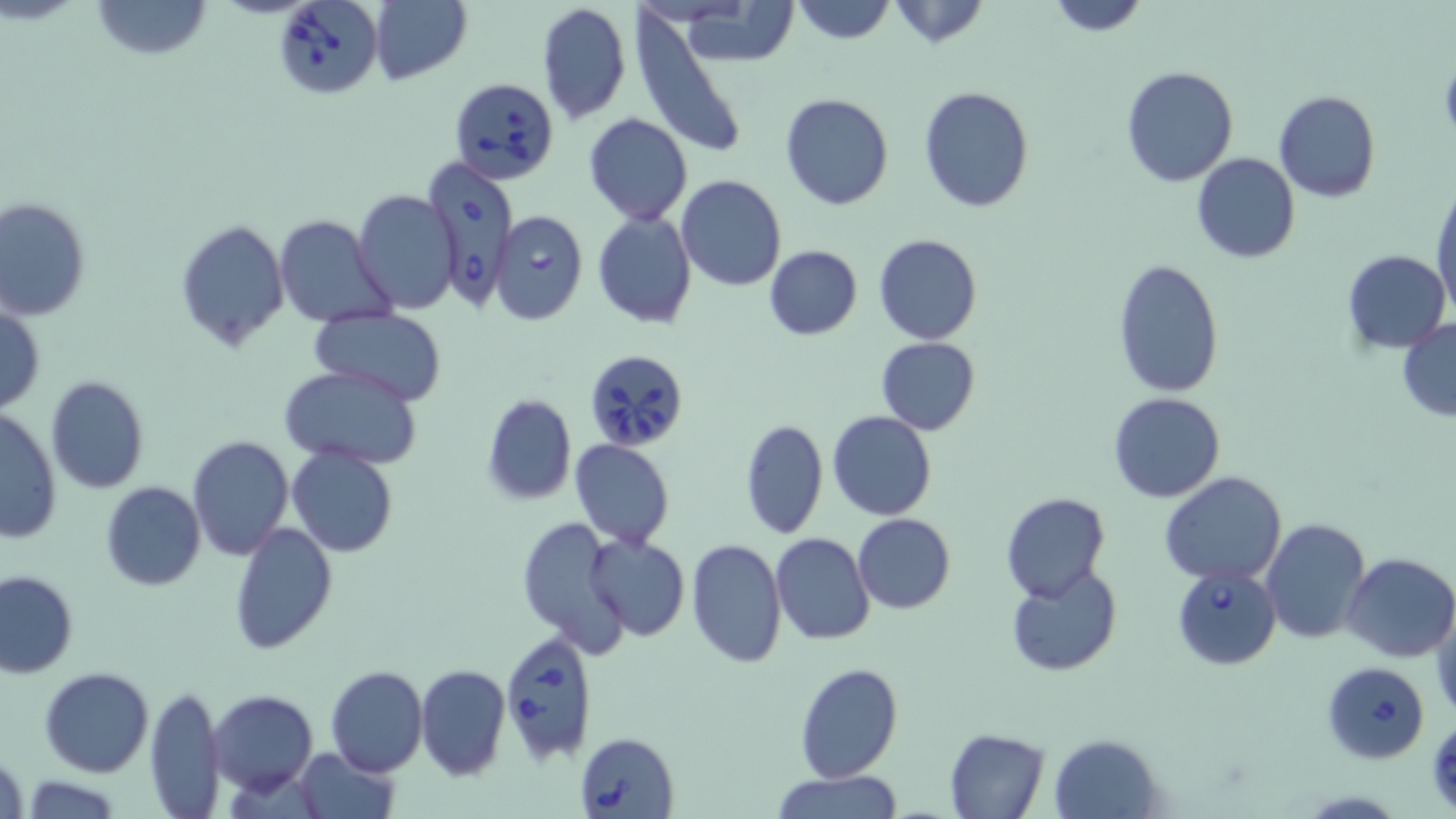

slide-level diagnosis = Babesia divergens
magnification = 1000x
preparation = thin blood film
image size = 1456×819 pixels
uninfected red blood cell locations = approximate bounding boxes as [x1, y1, x2, y2] in pixels: [92, 0, 212, 60], [1043, 0, 1150, 37], [369, 1, 472, 85], [789, 1, 898, 46], [885, 1, 991, 49], [536, 2, 632, 125], [674, 4, 801, 67], [633, 15, 748, 161], [1120, 65, 1238, 185], [918, 85, 1034, 213], [1272, 91, 1381, 204], [779, 94, 894, 211], [583, 113, 693, 225], [1191, 152, 1299, 263], [676, 176, 786, 292], [1431, 185, 1456, 318], [353, 190, 460, 313], [0, 197, 91, 320], [592, 212, 697, 329], [272, 214, 397, 327], [174, 219, 290, 350], [873, 233, 983, 345], [764, 245, 862, 340], [1343, 249, 1450, 353], [1114, 258, 1224, 400], [0, 305, 45, 414], [310, 309, 445, 403], [1397, 319, 1456, 420], [874, 337, 982, 435], [854, 339, 963, 507], [279, 364, 422, 468], [43, 375, 150, 494], [1107, 391, 1225, 503], [481, 394, 577, 504], [0, 409, 62, 542], [827, 411, 936, 522], [740, 417, 828, 540], [186, 435, 294, 560], [570, 439, 675, 549], [285, 444, 401, 559], [1160, 471, 1288, 585], [100, 482, 205, 591], [1001, 493, 1109, 604], [851, 513, 955, 613], [516, 516, 632, 657], [1262, 517, 1370, 645], [229, 522, 336, 654], [770, 532, 876, 645], [583, 534, 690, 642], [685, 539, 787, 667], [1344, 552, 1456, 662], [1006, 567, 1122, 676], [0, 571, 78, 678], [1431, 606, 1456, 724], [794, 663, 903, 783], [415, 664, 510, 781], [325, 665, 427, 778], [40, 667, 154, 777], [145, 683, 225, 816], [209, 690, 318, 794], [944, 728, 1050, 818], [1051, 733, 1163, 817], [1, 746, 27, 819], [293, 747, 401, 819], [772, 770, 903, 819], [19, 775, 125, 816]
Babesia divergens-infected red blood cell locations = approximate bounding boxes as [x1, y1, x2, y2] in pixels: [273, 0, 383, 99], [448, 74, 559, 183], [426, 157, 518, 310], [491, 212, 588, 324], [585, 348, 688, 453], [1172, 564, 1281, 668], [498, 632, 602, 767], [1323, 663, 1429, 762], [575, 731, 680, 818]
stain = May-Grünwald-Giemsa
field of view = single
modality = light microscopy